Classify this cell by malaria status.
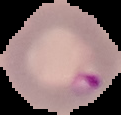

Parasitized.

Summary:
  - Preparation: thin blood smear
  - Image size: 121×115 pixels
  - Image type: segmented cell region on a black background